Classify this cell by malaria status.
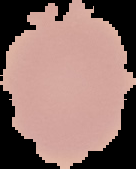

Uninfected.

Cell region segmented out of the field of view; the surrounding area is masked to black. From a thin blood smear. Image is 136×169 pixels.